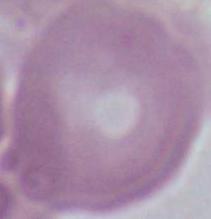

Summary:
  - Modality: photomicrograph
  - Identification: erythrocyte
  - Magnification: 1000x